Describe the morphology of the red blood cells.
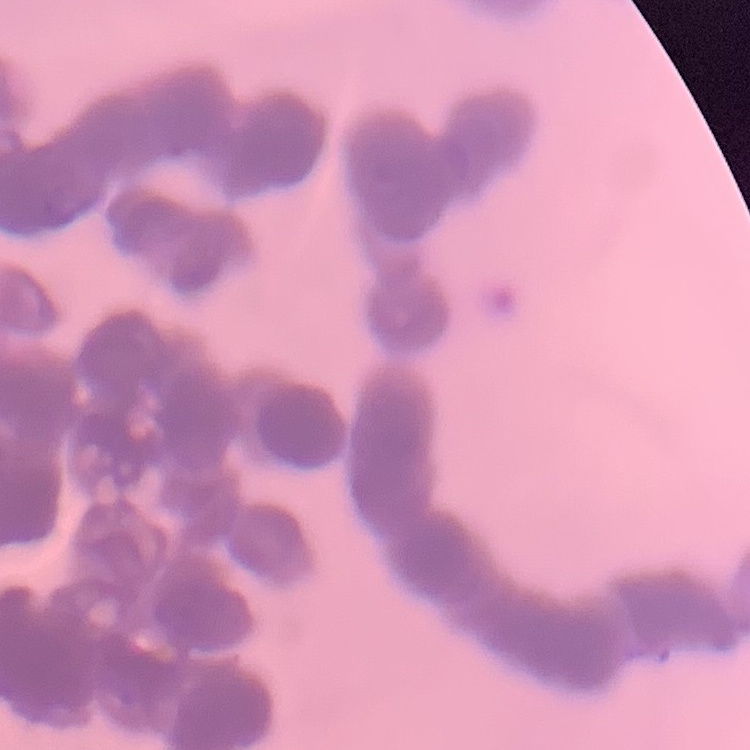

They show rouleaux formation.

preparation = thin blood smear
stain = Field's or Giemsa
image type = square crop of a larger photomicrograph